Give the position of every Plasmodium parasite.
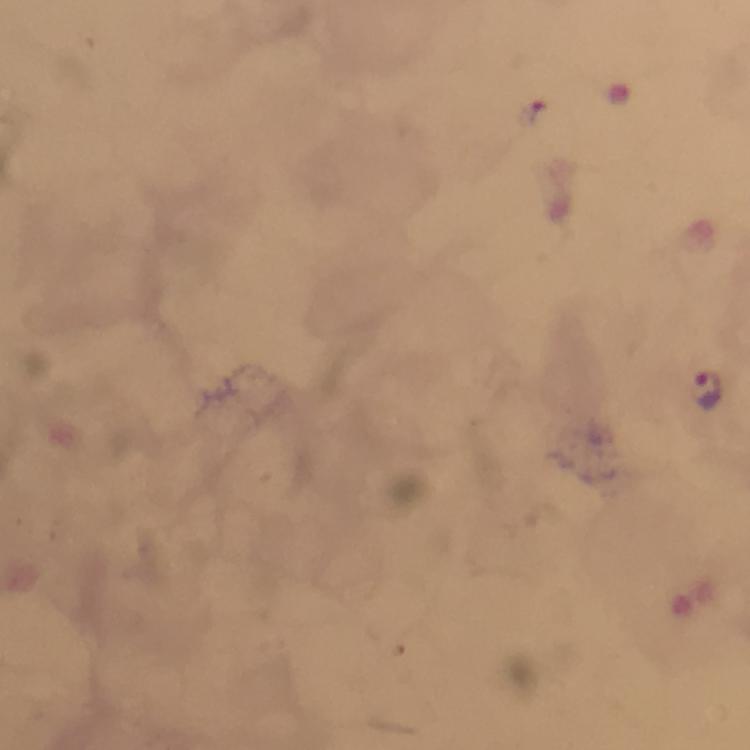
Approximate centers as (x, y) in pixels.
Plasmodium parasites: (708, 390).

At 100x magnification. Giemsa-stained preparation. From a malaria diagnostic workup. Cropped region of a single field of view. Photographed through the microscope with a smartphone camera. Thick blood smear. Immersion oil was used. Image is 750×750 pixels.